Identify the cell.
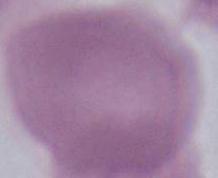

This is an erythrocyte.

modality = micrograph
magnification = 1000x